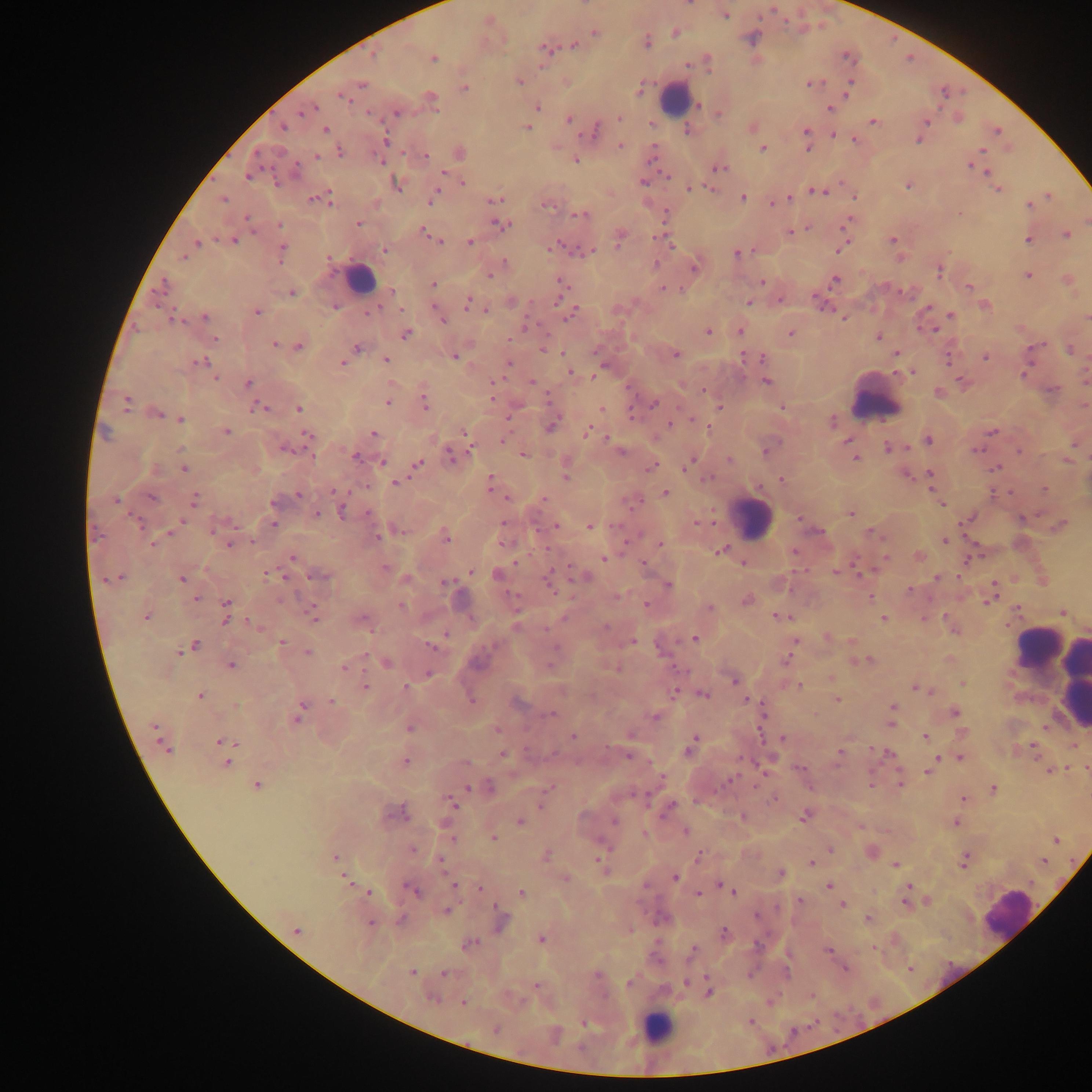

Approximate centers as {x, y} in pixels.
Summary:
  - Plasmodium parasite locations: {690, 4}, {725, 15}, {487, 20}, {675, 32}, {595, 33}, {646, 42}, {574, 45}, {545, 47}, {433, 57}, {848, 57}, {707, 61}, {519, 81}, {566, 81}, {360, 83}, {811, 83}, {464, 88}, {639, 89}, {847, 92}, {342, 96}, {431, 99}, {697, 104}, {536, 107}, {830, 107}, {307, 109}, {396, 112}, {719, 113}, {619, 117}, {569, 119}, {872, 120}, {926, 121}, {283, 126}, {527, 127}, {325, 128}, {751, 128}, {686, 129}, {594, 130}, {997, 130}, {806, 132}, {833, 133}, {918, 138}, {855, 139}, {384, 140}, {619, 145}, {806, 147}, {762, 148}, {980, 150}, {340, 152}, {460, 153}, {316, 156}, {424, 156}, {575, 159}, {381, 161}, {972, 164}, {718, 167}, {985, 171}, {442, 172}, {248, 174}, {667, 175}, {644, 182}, {396, 183}, {463, 183}, {908, 185}, {689, 188}, {709, 189}, {998, 189}, {814, 191}, {433, 195}, {1047, 195}, {854, 196}, {743, 197}, {789, 197}, {313, 198}, {222, 199}, {327, 199}, {497, 199}, {545, 203}, {772, 203}, {1029, 204}, {958, 213}, {580, 215}, {246, 217}, {358, 224}, {499, 224}, {846, 224}, {279, 225}, {806, 228}, {789, 232}, {426, 233}, {1066, 234}, {619, 237}, {232, 239}, {1028, 239}, {436, 240}, {893, 240}, {469, 242}, {195, 243}, {840, 248}, {383, 249}, {281, 251}, {585, 251}, {736, 254}, {184, 256}, {328, 257}, {504, 263}, {654, 265}, {694, 266}, {938, 269}, {489, 274}, {1027, 275}, {835, 279}, {1067, 279}, {760, 282}, {562, 283}, {433, 284}, {968, 287}, {663, 288}, {561, 290}, {391, 291}, {291, 292}, {780, 299}, {511, 301}, {468, 302}, {748, 302}, {820, 302}, {984, 305}, {335, 306}, {401, 310}, {486, 310}, {256, 311}, {570, 313}, {951, 315}, {204, 316}, {1087, 317}, {171, 318}, {844, 318}, {442, 319}, {935, 329}, {739, 330}, {708, 331}, {405, 333}, {790, 334}, {876, 336}, {214, 338}, {274, 344}, {298, 346}, {356, 348}, {543, 349}, {1070, 350}, {897, 352}, {562, 353}, {676, 354}, {454, 356}, {985, 356}, {743, 357}, {762, 358}, {385, 359}, {949, 359}, {198, 362}, {508, 362}, {343, 363}, {913, 371}, {570, 372}, {1024, 373}, {592, 376}, {216, 377}, {766, 381}, {494, 382}, {531, 382}, {963, 382}, {247, 384}, {704, 391}, {937, 393}, {491, 396}, {388, 401}, {126, 402}, {425, 402}, {654, 403}, {261, 407}, {719, 407}, {781, 407}, {299, 408}, {601, 408}, {155, 413}, {632, 415}, {179, 419}, {692, 419}, {832, 422}, {551, 425}, {670, 425}, {708, 428}, {225, 431}, {587, 431}, {992, 431}, {465, 432}, {372, 434}, {308, 435}, {468, 438}, {928, 439}, {503, 440}, {847, 440}, {1075, 442}, {888, 446}, {284, 447}, {976, 449}, {620, 451}, {766, 451}, {1020, 451}, {312, 454}, {452, 454}, {523, 454}, {356, 457}, {855, 457}, {1066, 459}, {730, 460}, {382, 462}, {566, 463}, {688, 463}, {416, 464}, {651, 466}, {184, 467}, {997, 467}, {905, 474}, {930, 475}, {565, 477}, {781, 479}, {395, 483}, {490, 483}, {930, 483}, {1044, 489}, {333, 491}, {664, 492}, {298, 495}, {151, 497}, {506, 497}, {543, 498}, {194, 499}, {115, 500}, {273, 502}, {941, 504}, {343, 510}, {315, 513}, {850, 513}, {1021, 517}, {800, 518}, {968, 518}, {696, 523}, {272, 524}, {503, 524}, {1061, 524}, {556, 525}, {589, 526}, {218, 527}, {820, 531}, {170, 532}, {871, 533}, {444, 536}, {376, 537}, {945, 540}, {230, 542}, {504, 543}, {659, 544}, {720, 551}, {794, 551}, {919, 556}, {292, 557}, {885, 558}, {970, 558}, {604, 559}, {643, 563}, {743, 563}, {384, 567}, {470, 571}, {836, 572}, {268, 573}, {319, 574}, {498, 575}, {583, 576}, {116, 577}, {182, 578}, {937, 578}, {1013, 578}, {406, 579}, {549, 579}, {1042, 580}, {446, 583}, {667, 584}, {993, 588}, {910, 589}, {617, 595}, {870, 597}, {195, 599}, {990, 599}, {745, 600}, {402, 605}, {646, 605}, {710, 608}, {1017, 609}, {226, 611}, {1061, 611}, {313, 614}, {147, 616}, {781, 617}, {361, 619}, {883, 619}, {254, 625}, {827, 637}, {694, 638}, {794, 640}, {852, 640}, {633, 641}, {282, 642}, {188, 647}, {432, 647}, {307, 653}, {787, 659}, {866, 660}, {857, 661}, {386, 662}, {230, 665}, {344, 667}, {427, 673}, {831, 678}, {734, 679}, {962, 683}, {365, 685}, {799, 686}, {916, 687}, {405, 688}, {928, 689}, {676, 692}, {702, 694}, {200, 695}, {471, 699}, {746, 699}, {836, 699}, {332, 701}, {892, 708}, {954, 712}, {298, 714}, {550, 714}, {763, 715}, {655, 716}, {891, 723}, {409, 727}, {497, 729}, {573, 735}, {924, 736}, {782, 739}, {692, 741}, {163, 743}, {223, 744}, {1073, 745}, {1033, 747}, {870, 748}, {690, 749}, {840, 751}, {887, 753}, {502, 754}, {628, 755}, {960, 757}, {953, 758}, {404, 761}, {936, 761}, {227, 762}, {799, 768}, {1086, 769}, {1048, 770}, {928, 771}, {900, 783}, {256, 785}, {869, 785}, {468, 787}, {489, 788}, {549, 790}, {993, 790}, {775, 797}, {964, 799}, {451, 801}, {543, 801}, {668, 807}, {398, 813}, {804, 815}, {742, 816}, {519, 821}, {614, 821}, {955, 822}, {684, 831}, {492, 837}, {1056, 840}, {412, 849}, {830, 849}, {872, 852}, {544, 855}, {698, 856}, {334, 857}, {439, 861}, {964, 861}, {1043, 861}, {599, 862}, {812, 862}, {896, 865}, {780, 874}, {674, 877}, {564, 878}, {346, 879}, {454, 885}, {720, 885}, {725, 886}, {829, 886}, {908, 887}, {480, 888}, {413, 890}, {368, 891}, {733, 891}, {521, 893}, {698, 893}, {799, 900}, {926, 901}, {906, 903}, {842, 905}, {446, 910}, {868, 919}, {500, 921}, {369, 923}, {296, 929}, {724, 933}, {540, 939}, {468, 944}, {873, 948}, {693, 950}, {828, 951}, {845, 968}, {412, 972}, {443, 973}, {686, 982}, {629, 984}, {536, 985}, {709, 992}, {432, 997}, {463, 1002}, {750, 1020}, {584, 1023}, {495, 1028}
  - Leukocyte locations: {674, 99}, {359, 279}, {876, 398}, {751, 519}, {1037, 646}, {1052, 665}, {1071, 676}, {1009, 914}, {656, 1028}
  - Image size: 1092×1092 pixels
  - Field of view: single
  - Country: Ghana
  - Preparation: thick blood smear
  - Capture: mobile-phone photograph through a microscope